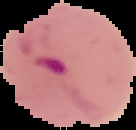
Summary:
  - Preparation: thin blood film
  - Malaria status: parasitized
  - Image size: 136×130 pixels
  - Image type: segmented cell region with the area outside set to black